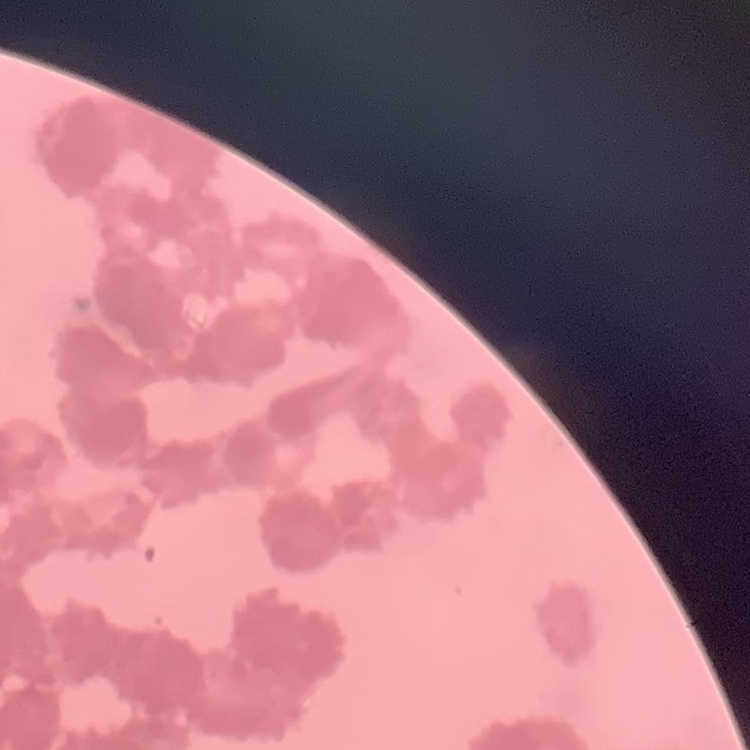

The red blood cells exhibit rouleaux formation. Thin peripheral smear. One tile cut from a larger photomicrograph. Stained with either Field's or Giemsa.